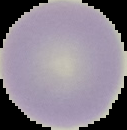

image size = 127×130 pixels
result = no malaria parasites detected
preparation = thin blood film
image type = segmented cell region with the area outside set to black